Identify the cell.
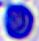

This is a leukocyte.

Summary:
  - Modality: micrograph
  - Magnification: 400x